Identify the blood parasite species.
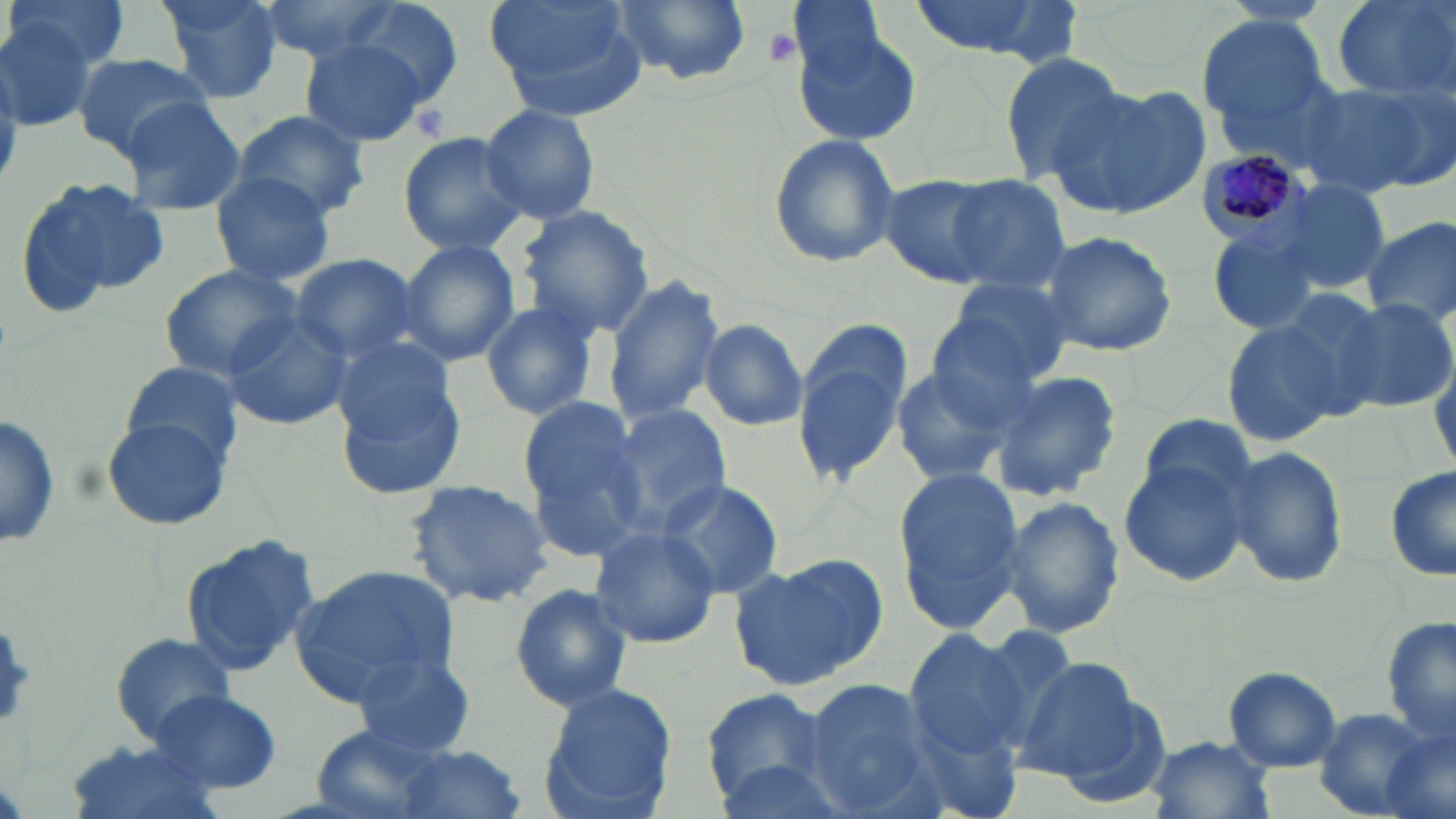

Plasmodium malariae.

field of view = one of a larger specimen
modality = optical microscopy
image size = 1456×819 pixels
platelet locations = approximate bounding boxes as (x1,y1)-(x2,y2) corner pairs in pixels: (761,27)-(802,69)
preparation = thin blood film
stain = May-Grünwald-Giemsa
uninfected red blood cell locations = approximate bounding boxes as (x1,y1)-(x2,y2) corner pairs in pixels: (4,0)-(133,72), (155,0)-(285,105), (257,0)-(416,64), (482,0)-(649,116), (610,0)-(750,86), (907,0)-(1073,62), (1330,0)-(1453,100), (346,2)-(464,110), (0,4)-(111,128), (1195,12)-(1333,141), (795,25)-(922,149), (298,39)-(433,149), (69,49)-(213,162), (999,49)-(1131,185), (1304,77)-(1450,196), (1057,82)-(1214,219), (119,98)-(248,217), (477,104)-(600,224), (228,109)-(370,224), (397,131)-(531,258), (768,133)-(899,268), (211,172)-(336,287), (878,174)-(1007,288), (15,176)-(167,315), (943,178)-(1073,294), (1275,179)-(1392,295), (514,205)-(655,339), (1361,217)-(1456,331), (1038,230)-(1178,358), (397,238)-(520,366), (289,253)-(423,366), (158,264)-(303,382), (604,275)-(726,430), (938,275)-(1076,389), (1337,294)-(1456,416), (480,301)-(598,421), (220,309)-(353,431), (1219,316)-(1352,448), (698,318)-(809,431), (793,324)-(911,488), (332,334)-(469,498), (121,358)-(248,466), (893,364)-(1017,487), (987,368)-(1123,502), (517,398)-(653,556), (609,403)-(732,533), (0,407)-(61,549), (100,416)-(233,532), (1119,436)-(1261,586), (1226,445)-(1350,589), (1387,463)-(1456,586), (891,467)-(1027,631), (401,477)-(554,611), (655,477)-(786,599), (998,496)-(1124,638), (589,525)-(722,649), (179,531)-(318,678), (731,552)-(888,691), (291,564)-(460,704), (510,584)-(633,711), (1386,613)-(1456,750), (902,629)-(1032,759), (111,631)-(235,744), (350,649)-(479,759), (1014,655)-(1150,783), (1224,667)-(1344,772), (799,676)-(944,816), (537,681)-(676,817), (698,688)-(837,809), (147,690)-(285,796), (1310,706)-(1446,819), (309,724)-(464,819), (1145,734)-(1273,818), (62,741)-(225,819), (383,743)-(528,819)
magnification = 1000x
Plasmodium malariae-infected red blood cell locations = approximate bounding boxes as (x1,y1)-(x2,y2) corner pairs in pixels: (1196,147)-(1320,264)